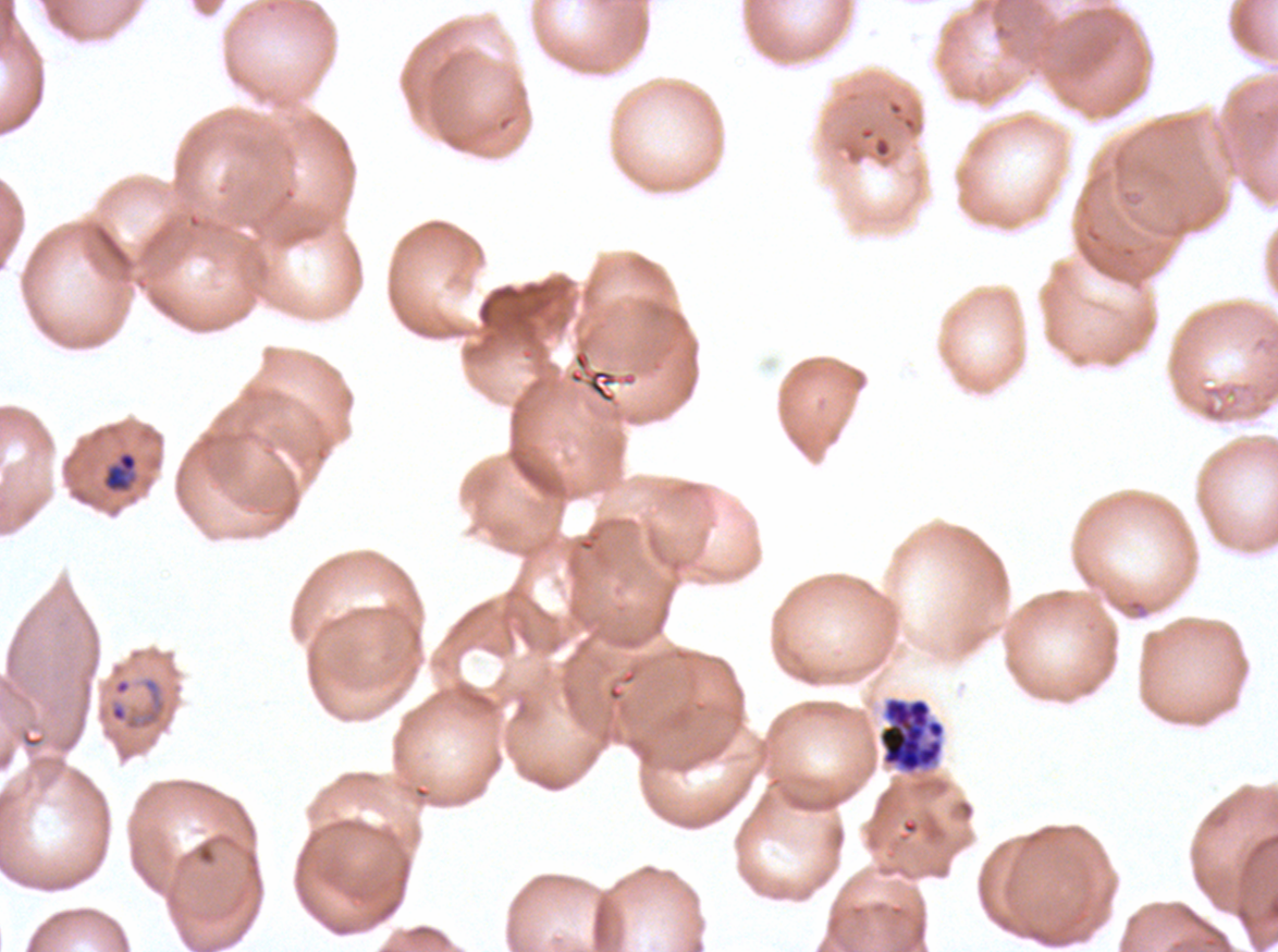
Approximate bounding boxes as {x1, y1, x2, y2} in pixels.
Summary:
  - Segmenter locations: {878, 696, 946, 774}
  - Ring locations: {108, 677, 166, 731}
  - Late-ring/early-trophozoite locations: {103, 451, 138, 492}
  - Stain: Giemsa
  - Preparation: thin blood smear
  - Field of view: sub-image separated from a larger composite
  - Image size: 1278×952 pixels
  - Specimen: P. falciparum from a patient in The Gambia, cultured ex vivo for 24 to 48 hours
  - Life-cycle stages observed: ring, late-ring/early-trophozoite, segmenter